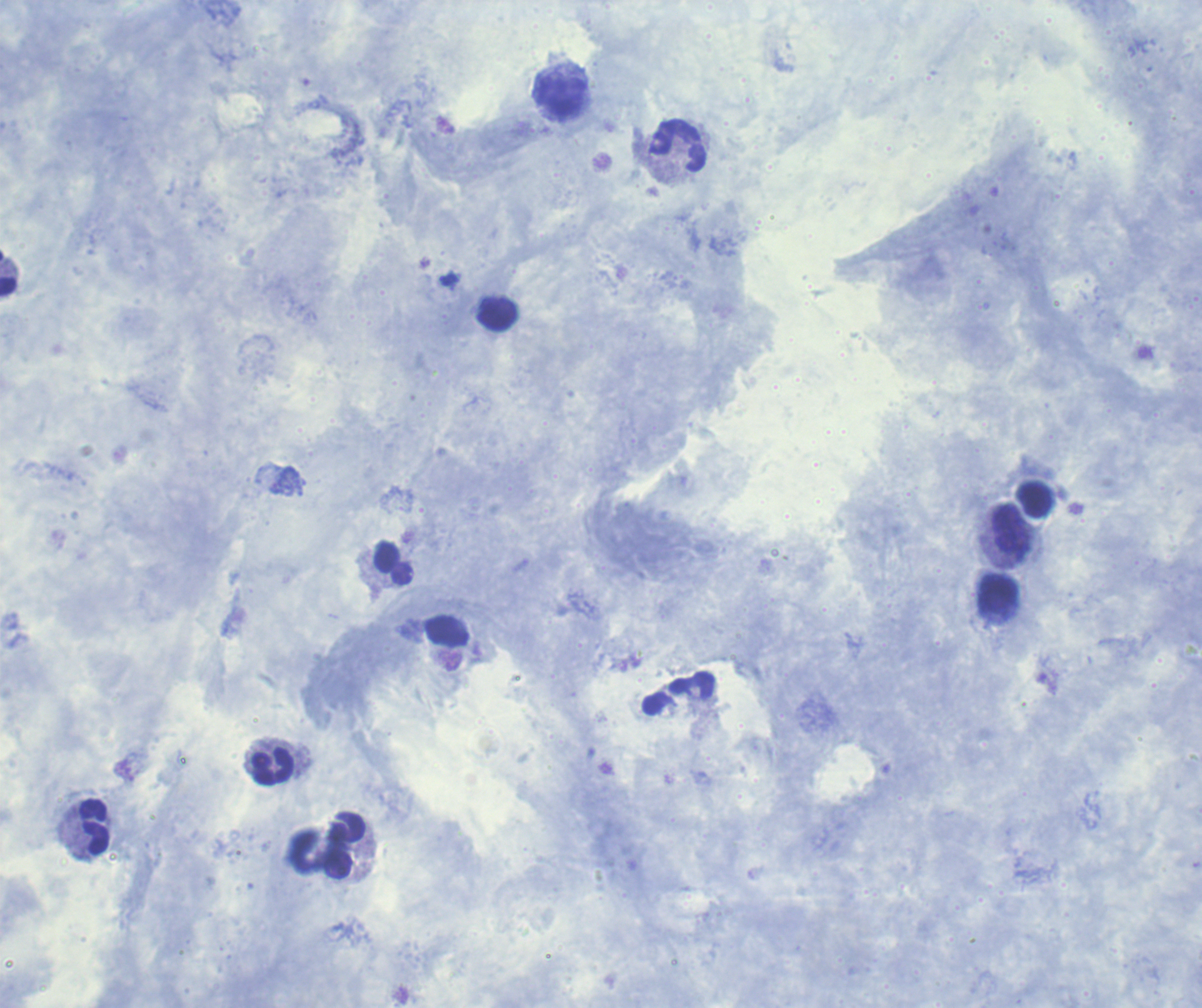

coordinate format = approximate centers as [x, y] in pixels
leukocyte locations = [560, 97], [678, 147], [8, 275], [496, 314], [1033, 499], [1011, 529], [394, 563], [998, 596], [272, 767], [94, 827], [344, 846]
magnification = 100x
result = no malaria parasites seen
context = previously used in an actual diagnosis
coloration quality = good
field of view = single
stain = Romanowsky
preparation = thick smear of blood
background quality = good
image size = 1202×1008 pixels